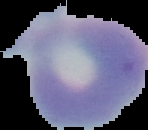
image type = cell region segmented out of the field of view; surrounding area masked to black
preparation = thin blood film
result = negative for Plasmodium parasites
image size = 148×130 pixels